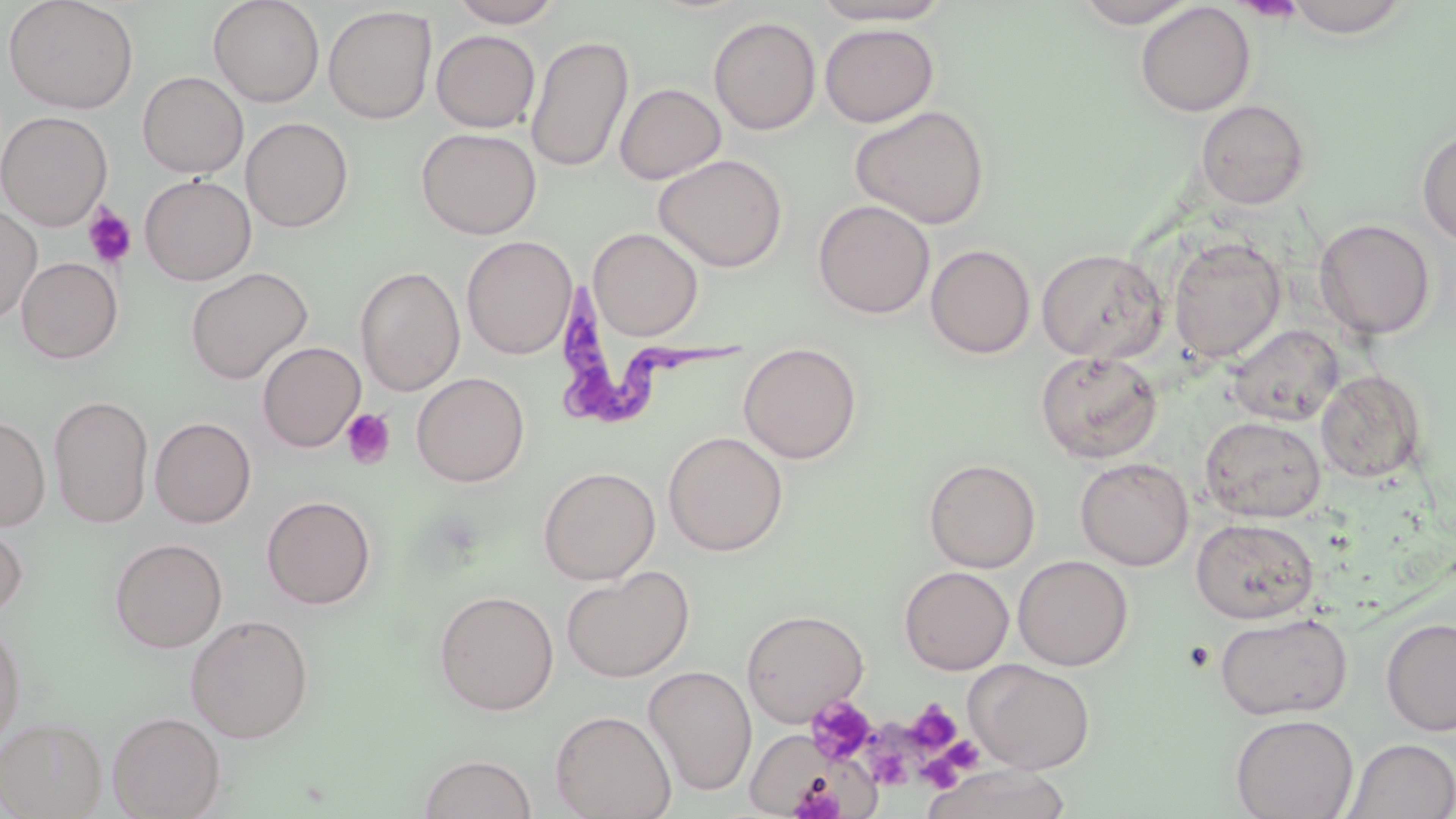

Summary:
  - Coordinate format: approximate bounding boxes as [x1, y1, x2, y2] in pixels
  - Trypanosoma brucei locations: [551, 277, 753, 427]
  - Uninfected red blood cell locations: [3, 0, 139, 114], [208, 0, 325, 108], [448, 0, 565, 28], [1073, 0, 1198, 28], [1281, 0, 1415, 38], [809, 1, 954, 26], [1134, 2, 1256, 117], [323, 5, 437, 124], [709, 16, 821, 135], [819, 22, 939, 127], [431, 30, 541, 133], [525, 34, 634, 173], [138, 71, 248, 178], [614, 83, 726, 184], [1195, 99, 1312, 210], [850, 105, 991, 229], [0, 110, 113, 230], [240, 117, 354, 232], [416, 127, 542, 239], [1416, 128, 1456, 247], [654, 153, 788, 272], [139, 174, 257, 285], [813, 199, 935, 319], [0, 206, 42, 325], [1314, 219, 1436, 339], [588, 227, 704, 341], [461, 235, 576, 359], [1168, 236, 1286, 363], [926, 244, 1036, 359], [1036, 247, 1168, 364], [16, 257, 123, 364], [355, 265, 465, 396], [185, 267, 313, 384], [1228, 324, 1343, 426], [737, 341, 863, 464], [257, 342, 366, 452], [1034, 350, 1162, 464], [1315, 369, 1427, 484], [411, 372, 530, 487], [49, 395, 153, 528], [0, 415, 50, 531], [1200, 416, 1327, 523], [150, 417, 256, 528], [663, 431, 788, 556], [1075, 457, 1193, 571], [923, 458, 1041, 573], [538, 466, 660, 585], [262, 495, 377, 610], [1190, 518, 1319, 624], [0, 521, 28, 621], [109, 537, 228, 654], [1013, 555, 1134, 671], [561, 566, 694, 684], [898, 566, 1014, 675], [433, 589, 559, 716], [741, 609, 870, 727], [1215, 612, 1353, 721], [185, 614, 314, 744], [1380, 617, 1456, 737], [0, 622, 26, 750], [965, 659, 1096, 775], [643, 665, 758, 797], [550, 710, 677, 819], [107, 711, 226, 819], [1230, 713, 1358, 819], [0, 717, 107, 819], [748, 733, 885, 818], [1343, 738, 1456, 818], [418, 752, 538, 818], [922, 764, 1073, 819]
  - Platelet locations: [1234, 1, 1306, 22], [82, 204, 138, 269], [341, 409, 396, 469], [807, 695, 878, 766], [904, 699, 962, 753], [918, 741, 984, 789], [867, 749, 911, 789], [788, 775, 845, 819]
  - Slide-level diagnosis: Trypanosoma brucei
  - Stain: May-Grünwald-Giemsa
  - Image size: 1456×819 pixels
  - Field of view: single
  - Modality: optical microscopy
  - Preparation: thin blood film
  - Magnification: 1000x